Assess this cell for malaria.
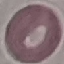
Uninfected.

Summary:
  - Stain: Giemsa
  - Image type: automatically extracted cell patch, resized to 64 × 64 pixels
  - Preparation: thin blood film
  - Capture: smartphone camera at the microscope eyepiece